State the blood parasite species.
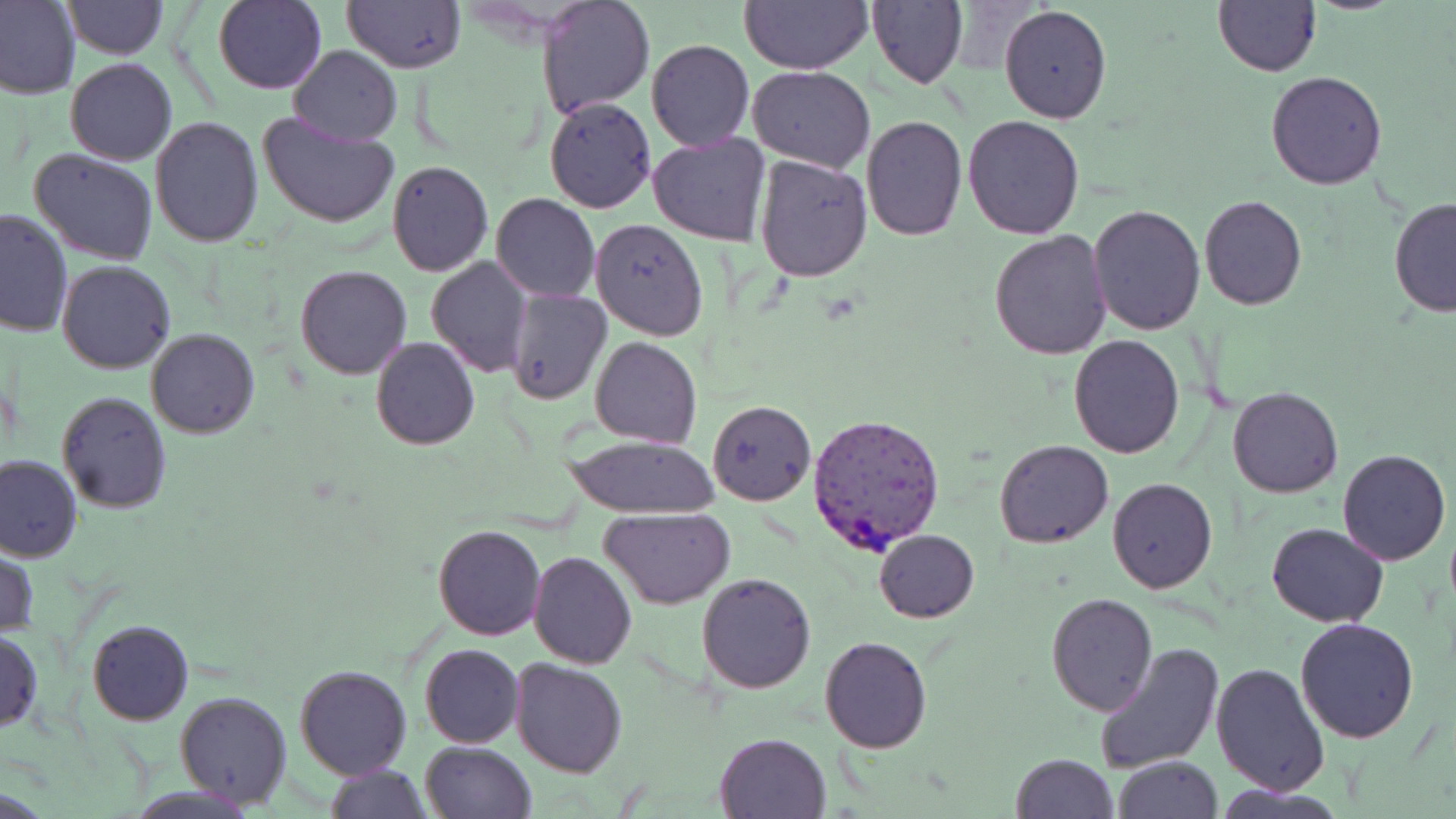

Plasmodium vivax.

Summary:
  - Coordinate format: approximate bounding boxes as named x1/y1/x2/y2 corners in pixels
  - Uninfected red blood cell locations: (x1=0, y1=0, x2=81, y2=100), (x1=61, y1=0, x2=166, y2=58), (x1=215, y1=0, x2=326, y2=93), (x1=537, y1=0, x2=655, y2=120), (x1=1214, y1=0, x2=1320, y2=76), (x1=343, y1=1, x2=464, y2=71), (x1=740, y1=1, x2=873, y2=73), (x1=868, y1=2, x2=967, y2=89), (x1=999, y1=5, x2=1111, y2=124), (x1=645, y1=38, x2=754, y2=152), (x1=290, y1=45, x2=402, y2=147), (x1=65, y1=59, x2=176, y2=165), (x1=748, y1=67, x2=875, y2=172), (x1=1266, y1=70, x2=1386, y2=189), (x1=544, y1=97, x2=656, y2=212), (x1=256, y1=110, x2=399, y2=230), (x1=151, y1=115, x2=263, y2=246), (x1=860, y1=116, x2=967, y2=240), (x1=963, y1=116, x2=1086, y2=239), (x1=647, y1=133, x2=772, y2=246), (x1=30, y1=148, x2=158, y2=264), (x1=754, y1=155, x2=873, y2=281), (x1=387, y1=160, x2=494, y2=276), (x1=491, y1=193, x2=599, y2=302), (x1=1199, y1=196, x2=1307, y2=310), (x1=1389, y1=199, x2=1456, y2=317), (x1=1087, y1=204, x2=1207, y2=336), (x1=1, y1=207, x2=75, y2=337), (x1=590, y1=217, x2=709, y2=340), (x1=988, y1=228, x2=1112, y2=360), (x1=426, y1=255, x2=532, y2=376), (x1=57, y1=260, x2=176, y2=373), (x1=295, y1=265, x2=413, y2=379), (x1=505, y1=289, x2=610, y2=404), (x1=145, y1=328, x2=261, y2=439), (x1=1068, y1=334, x2=1183, y2=459), (x1=590, y1=336, x2=702, y2=448), (x1=370, y1=337, x2=480, y2=451), (x1=1227, y1=386, x2=1343, y2=497), (x1=56, y1=390, x2=173, y2=513), (x1=707, y1=399, x2=815, y2=505), (x1=561, y1=434, x2=721, y2=518), (x1=993, y1=440, x2=1113, y2=549), (x1=1337, y1=449, x2=1451, y2=565), (x1=0, y1=454, x2=81, y2=562), (x1=1107, y1=478, x2=1217, y2=592), (x1=600, y1=507, x2=735, y2=608), (x1=1267, y1=522, x2=1389, y2=628), (x1=433, y1=525, x2=545, y2=641), (x1=873, y1=529, x2=980, y2=623), (x1=1, y1=544, x2=38, y2=641), (x1=528, y1=551, x2=637, y2=669), (x1=696, y1=573, x2=816, y2=694), (x1=1046, y1=593, x2=1156, y2=714), (x1=1295, y1=616, x2=1420, y2=742), (x1=87, y1=619, x2=193, y2=726), (x1=0, y1=627, x2=43, y2=735), (x1=820, y1=636, x2=933, y2=754), (x1=1096, y1=642, x2=1223, y2=774), (x1=420, y1=643, x2=524, y2=748), (x1=510, y1=658, x2=628, y2=777), (x1=1210, y1=661, x2=1329, y2=798), (x1=294, y1=664, x2=412, y2=779), (x1=173, y1=690, x2=292, y2=809), (x1=714, y1=732, x2=833, y2=819), (x1=419, y1=741, x2=537, y2=819), (x1=1011, y1=752, x2=1119, y2=819), (x1=1113, y1=756, x2=1222, y2=819), (x1=325, y1=762, x2=432, y2=819)
  - Plasmodium vivax-infected red blood cell locations: (x1=807, y1=412, x2=946, y2=553)
  - Preparation: thin blood smear
  - Stain: May-Grünwald-Giemsa
  - Field of view: one of a larger specimen
  - Magnification: 1000x
  - Image size: 1456×819 pixels
  - Modality: light microscopy